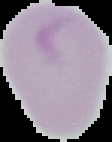

Image is 112×142 pixels. From a thin blood smear. Cell region segmented out of the field of view; the surrounding area is masked to black. Malaria status: uninfected.